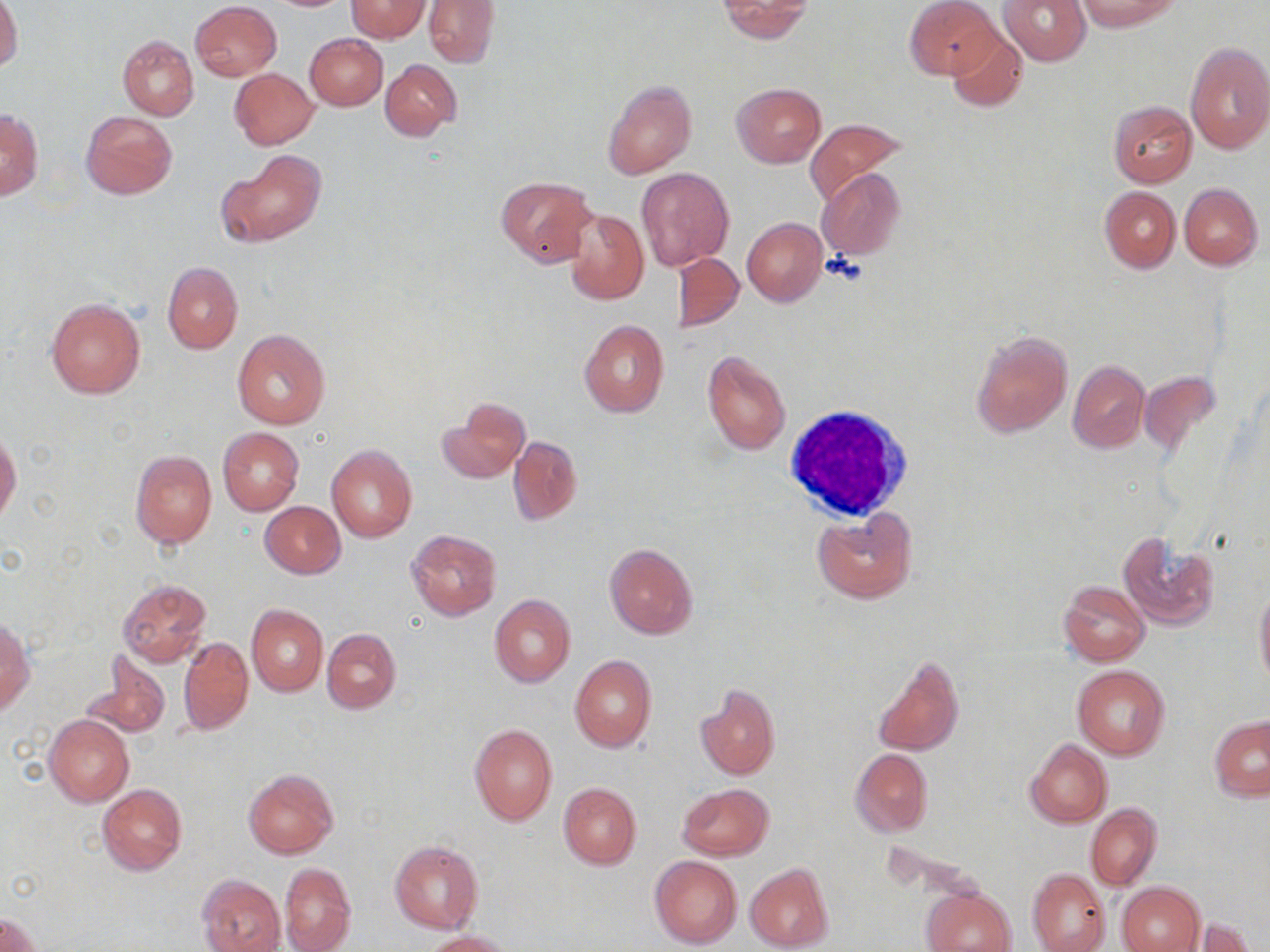
Approximate bounding boxes as (x1, y1, x2, y2) in pixels. White blood cell locations: (782, 403, 915, 524). Uninfected red blood cell locations: (0, 0, 23, 73), (422, 0, 498, 67), (717, 0, 816, 42), (906, 0, 1000, 81), (998, 0, 1090, 66), (1076, 0, 1180, 32), (344, 1, 430, 41), (190, 2, 281, 81), (946, 30, 1028, 115), (305, 34, 388, 110), (117, 35, 199, 119), (1184, 41, 1270, 155), (380, 58, 462, 140), (229, 68, 318, 150), (602, 79, 696, 177), (732, 83, 826, 167), (1108, 100, 1197, 188), (0, 108, 42, 201), (81, 111, 176, 200), (804, 119, 909, 207), (222, 147, 325, 245), (637, 167, 734, 270), (817, 168, 906, 262), (495, 177, 596, 267), (1179, 183, 1262, 269), (1099, 186, 1180, 272), (565, 207, 648, 304), (741, 216, 826, 306), (671, 251, 744, 332), (162, 261, 242, 353), (45, 297, 146, 399), (578, 319, 669, 418), (232, 328, 330, 429), (971, 329, 1072, 437), (701, 350, 792, 455), (1067, 360, 1149, 454), (1139, 370, 1221, 460), (440, 397, 530, 484), (218, 427, 303, 515), (0, 432, 22, 524), (509, 436, 582, 525), (326, 445, 417, 543), (130, 450, 216, 548), (260, 500, 345, 578), (812, 508, 917, 602), (405, 528, 502, 621), (1116, 531, 1220, 630), (605, 543, 698, 640), (117, 578, 212, 667), (1058, 580, 1149, 666), (1254, 584, 1270, 689), (489, 593, 576, 688), (246, 604, 327, 696), (0, 621, 34, 718), (322, 628, 401, 714), (178, 636, 253, 736), (80, 649, 170, 740), (569, 654, 657, 752), (871, 655, 965, 757), (1072, 665, 1170, 759), (695, 684, 780, 780), (44, 714, 134, 807), (1210, 715, 1269, 802), (469, 723, 557, 825), (1025, 738, 1112, 827), (850, 749, 933, 836), (243, 768, 338, 859), (98, 783, 187, 875), (558, 783, 641, 870), (676, 783, 774, 860), (1086, 803, 1161, 890), (390, 840, 483, 933), (649, 855, 742, 948), (280, 862, 355, 952), (744, 863, 835, 952), (1026, 867, 1111, 952), (197, 873, 286, 952), (1118, 881, 1205, 952), (923, 886, 1014, 952), (0, 910, 43, 952), (1192, 918, 1255, 952), (421, 930, 513, 952). Slide-level diagnosis: no evidence of blood parasites. One field of a larger specimen. Image is 1270×952 pixels. Light microscopy. Captured at 1000x magnification. May-Grünwald-Giemsa stain. Thin blood film.